Identify the parasite.
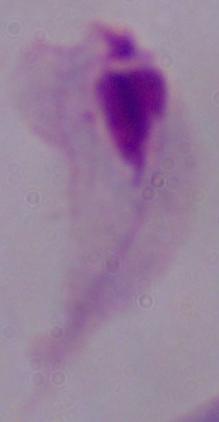

This is a trichomonad.

Summary:
  - Magnification: 1000x
  - Modality: photomicrograph